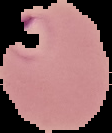

Result: Plasmodium parasites identified. From a thin blood smear. The area outside the segmented cell region is set to black. Image is 112×133 pixels.